Locate every blood parasite and identify its species.
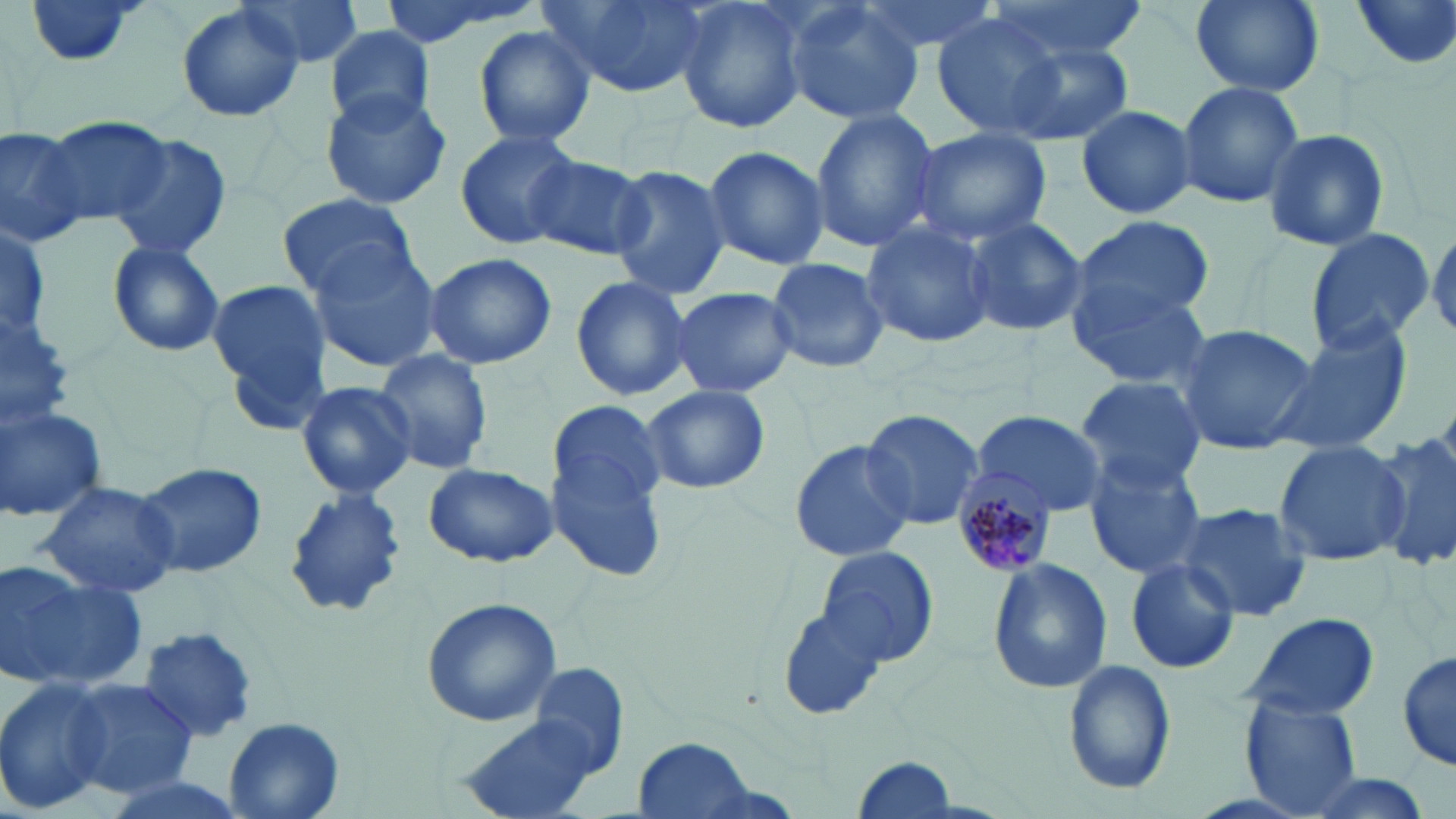
Approximate bounding boxes as (x1, y1, x2, y2) in pixels.
Plasmodium malariae-infected red blood cells: (946, 470, 1054, 579).
No Plasmodium falciparum, Plasmodium ovale, Plasmodium vivax, Babesia divergens, or Trypanosoma brucei observed.

Summary:
  - Uninfected red blood cell locations: (19, 0, 151, 69), (237, 0, 366, 70), (371, 0, 534, 48), (541, 0, 704, 99), (675, 0, 810, 136), (848, 0, 1001, 61), (981, 0, 1146, 58), (1349, 0, 1456, 74), (781, 1, 926, 126), (1191, 1, 1321, 95), (177, 2, 305, 124), (930, 13, 1071, 138), (324, 25, 436, 129), (474, 26, 595, 149), (1005, 38, 1136, 146), (1175, 80, 1304, 211), (321, 89, 452, 210), (1075, 103, 1199, 221), (808, 107, 939, 253), (40, 114, 171, 228), (0, 122, 89, 246), (908, 127, 1052, 247), (454, 129, 584, 249), (1262, 130, 1390, 249), (108, 133, 231, 260), (701, 144, 830, 271), (524, 153, 652, 261), (607, 167, 733, 300), (279, 193, 417, 300), (963, 215, 1087, 338), (1070, 215, 1214, 336), (860, 220, 995, 350), (0, 221, 52, 336), (1428, 224, 1456, 340), (1303, 227, 1433, 353), (107, 240, 226, 359), (305, 241, 444, 371), (422, 251, 556, 370), (766, 256, 888, 376), (570, 274, 694, 400), (206, 280, 331, 418), (666, 285, 799, 400), (1071, 285, 1211, 390), (0, 303, 77, 430), (1265, 319, 1413, 457), (1173, 321, 1320, 456), (371, 348, 494, 479), (1075, 375, 1207, 494), (294, 380, 416, 499), (643, 386, 770, 495), (549, 401, 667, 575), (0, 403, 108, 524), (862, 409, 986, 533), (974, 409, 1107, 516), (1371, 427, 1456, 575), (1271, 437, 1408, 567), (789, 439, 916, 563), (1083, 453, 1208, 579), (135, 463, 266, 578), (423, 463, 558, 567), (36, 479, 182, 600), (282, 487, 406, 618), (1172, 501, 1315, 623), (815, 546, 939, 666), (988, 558, 1113, 695), (1123, 558, 1241, 674), (0, 560, 148, 693), (421, 598, 561, 726), (776, 608, 887, 722), (1240, 611, 1382, 720), (138, 625, 260, 744), (1396, 648, 1454, 772), (1062, 659, 1173, 796), (64, 677, 197, 799), (0, 678, 113, 812), (1241, 698, 1362, 819), (454, 707, 611, 819), (224, 717, 345, 818), (627, 736, 764, 819), (850, 753, 958, 818), (1284, 770, 1438, 819)
  - Slide-level diagnosis: Plasmodium malariae
  - Preparation: thin blood film
  - Stain: May-Grünwald-Giemsa
  - Image size: 1456×819 pixels
  - Modality: light microscopy
  - Field of view: single
  - Magnification: 1000x